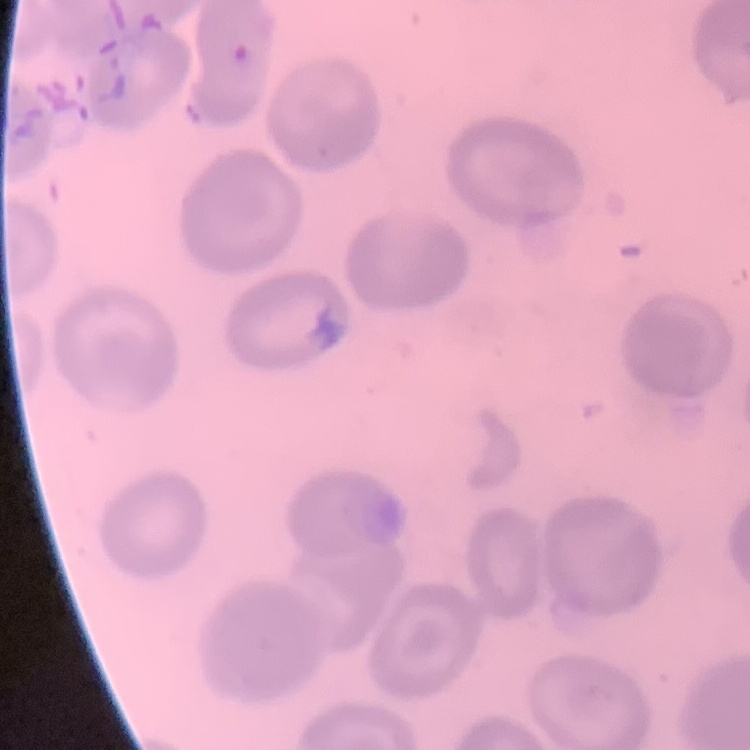
The erythrocytes show no rouleaux formation. Thin peripheral smear. One tile cut from a larger photomicrograph. Stained with either Field's or Giemsa.